Report the malaria status of this cell.
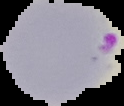
Parasitized.

image size = 124×106 pixels
preparation = thin blood smear
image type = cell region segmented out of the field of view; surrounding area masked to black